Point out each leukocyte.
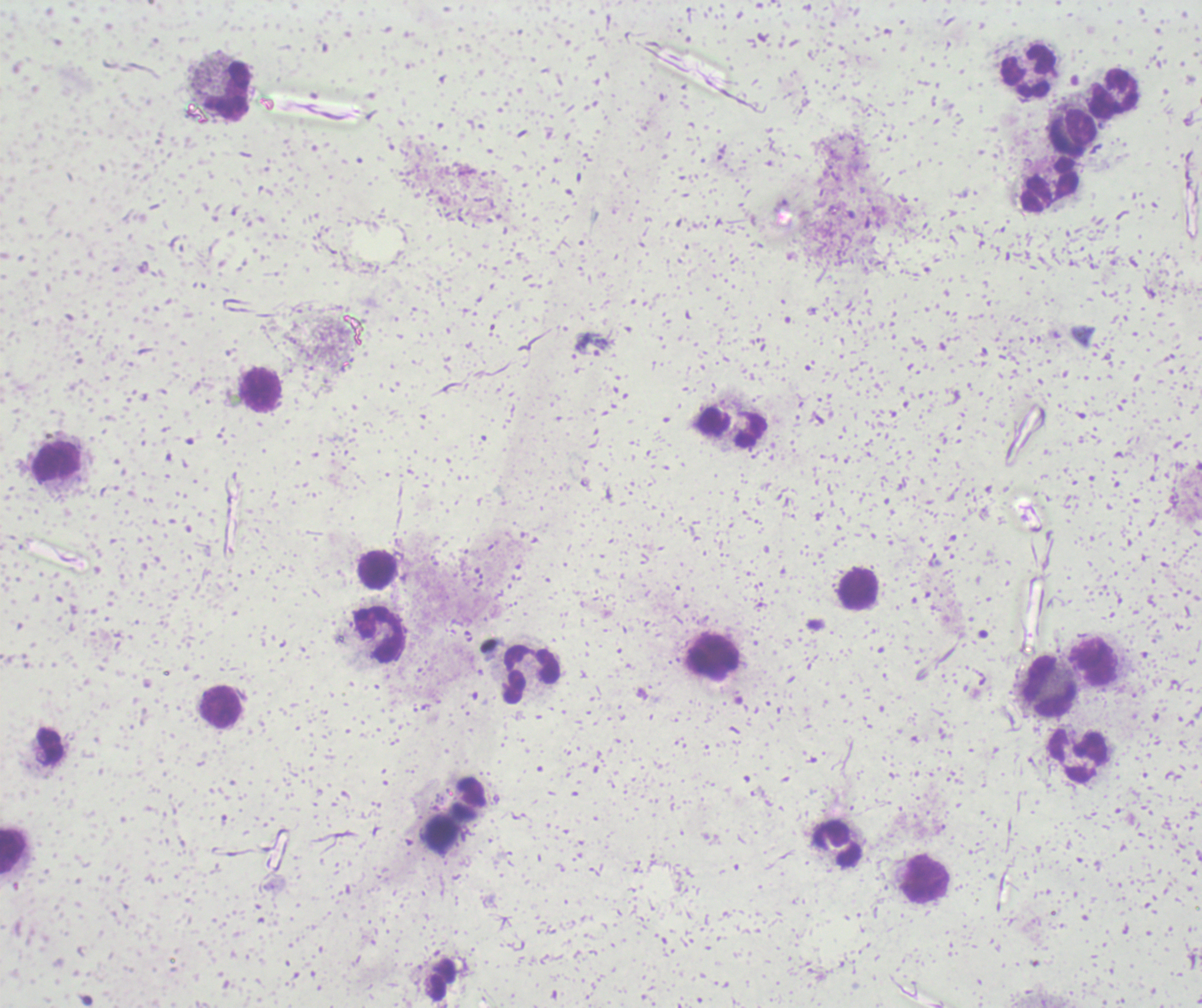

Approximate centers as [x, y] in pixels.
Leukocytes: [1027, 70], [227, 89], [1112, 92], [1071, 133], [1048, 186], [260, 390], [732, 426], [57, 463], [376, 570], [856, 588], [378, 635], [712, 656], [1091, 661], [530, 673], [1048, 686], [219, 707], [1077, 755], [441, 833], [836, 845], [12, 852], [924, 879].

coordinate format = approximate centers as [x, y] in pixels
trophozoite locations = [593, 344], [224, 821]
background quality = poor
field of view = single
context = previously used in a real diagnosis
stain = Romanowsky
preparation = thick blood smear
image size = 1202×1008 pixels
magnification = 100x
result = malaria parasites identified